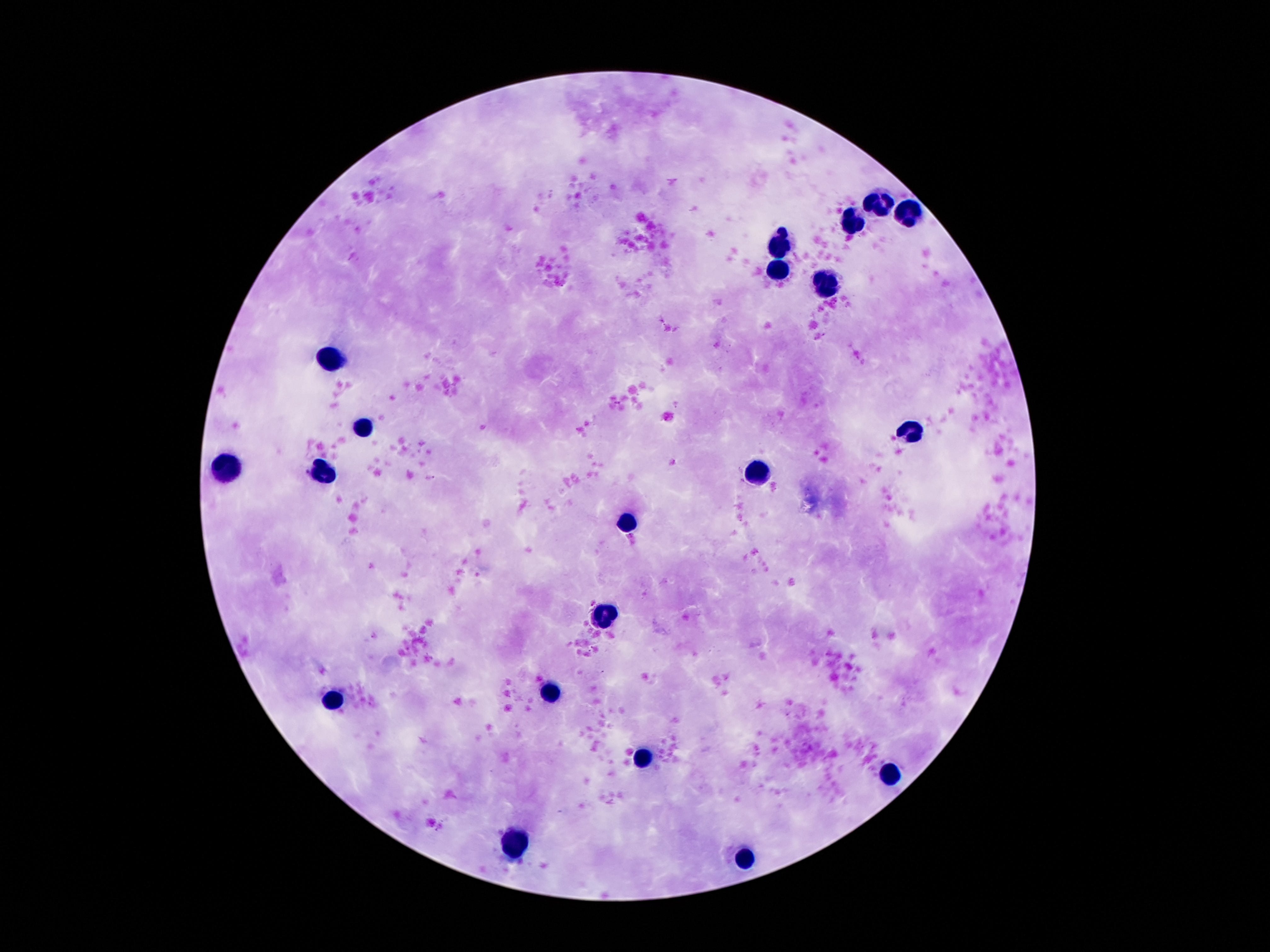

image_size: 1270×952 pixels
leukocyte_locations: 'approximate object centers, in pixels from the top-left corner: (x=876, y=200), (x=911, y=213), (x=850, y=220), (x=782, y=243), (x=776, y=273), (x=822, y=284), (x=326, y=360), (x=362, y=427), (x=909, y=429), (x=229, y=467), (x=323, y=467), (x=759, y=470), (x=626, y=523), (x=606, y=615), (x=550, y=694), (x=334, y=701), (x=647, y=755), (x=888, y=775), (x=517, y=843), (x=746, y=856)'
stain: Giemsa
preparation: thick blood film
patient_malaria_status: negative
magnification: 100x
field_of_view: one from this slide
capture: smartphone camera through the microscope eyepiece